Classify this cell by malaria status.
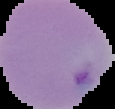

Parasitized.

From a thin blood film. Image is 115×109 pixels. Segmented cell region on a black background.